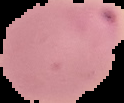
result: Plasmodium parasites detected
preparation: thin blood film
image_size: 124×103 pixels
image_type: segmented cell region with the area outside set to black